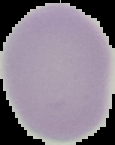
Malaria status: uninfected. Cell region segmented out of the field of view; the surrounding area is masked to black. From a thin blood smear. Image is 115×145 pixels.